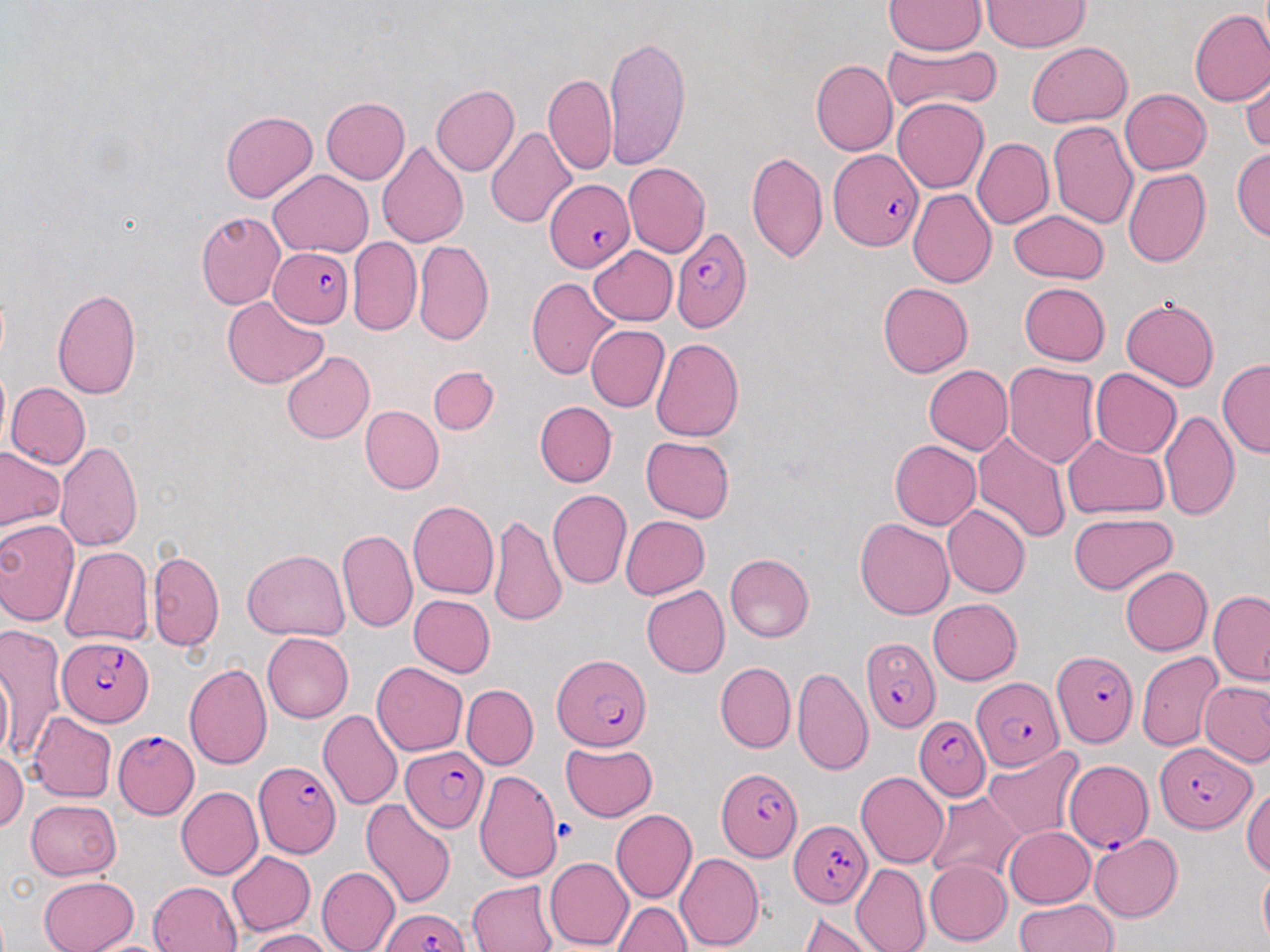
Summary:
  - Coordinate format: approximate bounding boxes as (x1,y1)-(x2,y2) corner pairs in pixels
  - Uninfected red blood cell locations: (982,0)-(1088,52), (883,1)-(984,55), (1189,9)-(1270,106), (603,33)-(690,170), (883,42)-(1001,114), (1026,42)-(1132,128), (811,59)-(896,156), (1240,61)-(1270,155), (544,72)-(615,175), (431,84)-(519,177), (1120,89)-(1210,175), (321,96)-(410,184), (892,97)-(989,194), (221,111)-(318,202), (1047,120)-(1138,229), (486,127)-(577,230), (972,138)-(1053,229), (375,141)-(469,248), (1231,147)-(1270,242), (746,151)-(828,265), (623,162)-(710,257), (1123,167)-(1211,268), (268,169)-(373,257), (907,189)-(997,288), (196,210)-(286,309), (1007,210)-(1109,284), (347,237)-(421,336), (414,240)-(493,344), (588,245)-(677,325), (525,276)-(620,379), (877,281)-(973,377), (1019,282)-(1110,365), (52,287)-(143,400), (221,296)-(329,389), (1121,296)-(1220,390), (586,325)-(670,412), (651,338)-(744,441), (282,351)-(374,443), (1218,358)-(1269,458), (1003,362)-(1101,469), (923,364)-(1013,454), (428,366)-(500,434), (1091,368)-(1182,458), (5,382)-(91,469), (535,401)-(617,486), (360,405)-(444,494), (1159,410)-(1240,521), (973,430)-(1070,542), (1061,433)-(1170,519), (641,436)-(735,522), (889,439)-(980,530), (55,440)-(143,551), (0,447)-(65,532), (547,489)-(632,590), (407,500)-(498,599), (943,505)-(1030,598), (489,513)-(566,627), (1068,513)-(1177,593), (621,515)-(709,598), (855,518)-(953,620), (0,519)-(80,626), (336,528)-(418,633), (60,546)-(153,646), (243,549)-(349,640), (147,550)-(223,651), (725,553)-(814,642), (1120,566)-(1212,654), (641,584)-(730,678), (1209,590)-(1270,686), (408,594)-(495,678), (928,598)-(1023,684), (1,625)-(65,763), (262,632)-(353,723), (1,650)-(14,768), (1136,652)-(1224,751), (371,662)-(467,755), (715,662)-(796,753), (184,664)-(271,769), (792,666)-(873,776), (1200,681)-(1270,767), (462,684)-(539,769), (318,710)-(403,809), (27,713)-(116,802), (560,742)-(656,822), (983,747)-(1084,841), (0,750)-(28,833), (472,772)-(561,877), (855,772)-(950,869), (1242,784)-(1270,877), (175,787)-(263,880), (927,791)-(1025,883), (361,798)-(456,909), (25,799)-(121,880), (611,809)-(697,904), (1005,826)-(1095,908), (1089,833)-(1182,922), (227,851)-(316,935), (675,852)-(764,951), (544,857)-(634,950), (925,859)-(1012,945), (851,863)-(931,952), (153,866)-(313,944), (316,866)-(400,952), (1258,866)-(1270,946), (39,876)-(139,952), (148,880)-(242,951), (468,880)-(557,952), (1013,900)-(1119,952), (613,902)-(692,952), (798,912)-(881,952), (246,928)-(334,952), (76,936)-(179,952)
  - Plasmodium falciparum-infected red blood cell locations: (829,150)-(922,251), (544,178)-(635,273), (671,227)-(751,333), (269,246)-(355,326), (860,634)-(937,734), (57,636)-(154,731), (1050,649)-(1138,748), (551,654)-(653,753), (971,676)-(1063,770), (914,716)-(990,801), (113,731)-(199,817), (1155,743)-(1255,832), (400,745)-(488,832), (1063,758)-(1152,851), (254,760)-(342,858), (717,767)-(801,862), (789,820)-(873,908), (380,908)-(469,952)
  - Slide-level diagnosis: Plasmodium falciparum
  - Magnification: 1000x
  - Field of view: one of a larger specimen
  - Image size: 1270×952 pixels
  - Preparation: thin blood smear
  - Stain: May-Grünwald-Giemsa
  - Modality: optical microscopy